Assess the morphology of the erythrocytes.
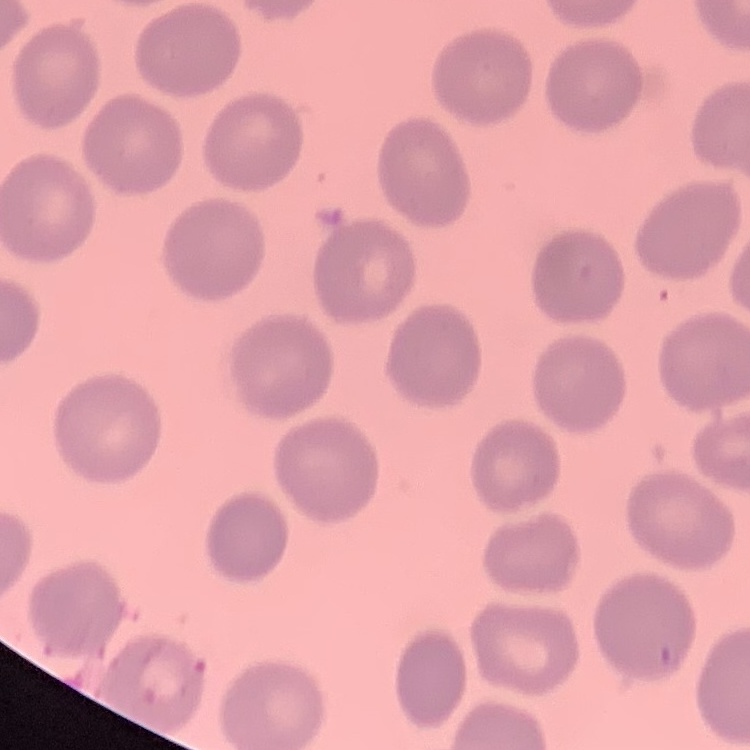

They show no rouleaux formation.

Summary:
  - Image type: one tile cut from a larger photomicrograph
  - Stain: Field's or Giemsa
  - Preparation: thin blood film